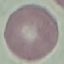
Malaria status: uninfected. Acquired by smartphone through the microscope eyepiece. Automatically extracted cell patch, resized to 64 × 64 pixels. Thin blood smear. Giemsa-stained preparation.